Classify this cell by malaria status.
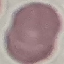

It is uninfected.

image type = automatically extracted cell patch, resized to 64 × 64 pixels
preparation = thin smear
capture = smartphone through the microscope eyepiece
stain = Giemsa